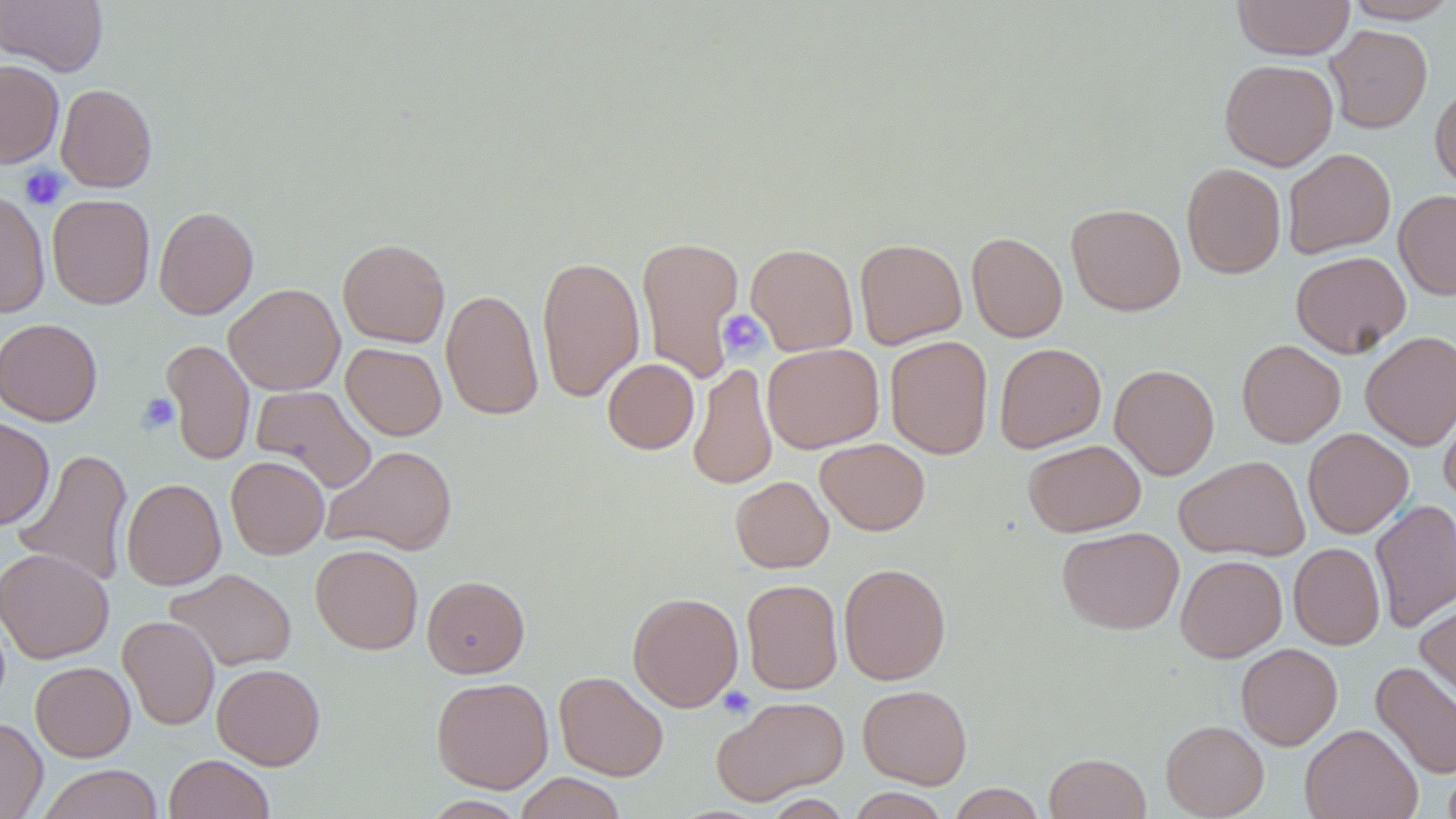
{
  "slide_level_diagnosis": "no evidence of blood parasites",
  "stain": "May-Grünwald-Giemsa",
  "platelet_locations": "approximate bounding boxes as (x1,y1)-(x2,y2) corner pairs in pixels: (19,165)-(69,211), (718,310)-(769,360), (136,393)-(179,433), (717,686)-(755,718)",
  "preparation": "thin blood film",
  "field_of_view": "single",
  "image_size": "1456×819 pixels",
  "magnification": "1000x",
  "uninfected_red_blood_cell_locations": "approximate bounding boxes as (x1,y1)-(x2,y2) corner pairs in pixels: (1,0)-(108,75), (1232,0)-(1355,59), (1342,0)-(1456,23), (1325,25)-(1432,133), (1219,59)-(1338,170), (0,60)-(64,168), (1430,83)-(1456,192), (56,84)-(157,192), (1282,148)-(1395,259), (1181,162)-(1286,279), (0,188)-(50,318), (1394,190)-(1456,300), (47,194)-(155,309), (1066,203)-(1186,316), (154,206)-(258,319), (966,231)-(1068,342), (636,235)-(744,382), (854,238)-(966,348), (338,239)-(450,347), (746,242)-(858,355), (1291,251)-(1411,358), (536,255)-(645,402), (224,283)-(344,395), (441,289)-(543,421), (0,318)-(103,426), (1360,332)-(1456,449), (884,335)-(993,459), (162,339)-(254,466), (1236,340)-(1346,447), (341,342)-(446,440), (762,343)-(884,452), (994,343)-(1106,452), (602,358)-(699,454), (688,362)-(777,491), (1109,363)-(1219,480), (251,385)-(376,493), (1439,396)-(1456,504), (0,416)-(55,530), (1303,428)-(1413,538), (815,438)-(930,535), (1023,439)-(1146,537), (323,445)-(457,556), (12,448)-(133,588), (1174,455)-(1309,561), (226,456)-(329,559), (730,476)-(833,573), (122,478)-(226,590), (1370,498)-(1456,634), (1057,526)-(1185,635), (1289,543)-(1385,650), (310,544)-(423,654), (0,547)-(114,664), (1176,554)-(1287,662), (838,562)-(951,685), (165,568)-(297,672), (422,575)-(530,678), (741,578)-(843,695), (627,592)-(743,711), (1415,596)-(1456,709), (118,615)-(220,730), (1235,643)-(1342,750), (1371,660)-(1456,780), (30,661)-(136,761), (212,663)-(325,769), (554,671)-(668,781), (431,676)-(553,793), (857,684)-(972,789), (712,695)-(849,805), (0,717)-(47,818), (1161,720)-(1269,819), (1300,724)-(1422,819), (1044,752)-(1151,818), (163,754)-(274,819), (1442,762)-(1456,819), (37,764)-(164,819), (515,772)-(626,819), (948,783)-(1047,819), (846,788)-(950,819), (762,794)-(852,818)",
  "modality": "optical microscopy"
}